Describe the morphology of the red blood cells.
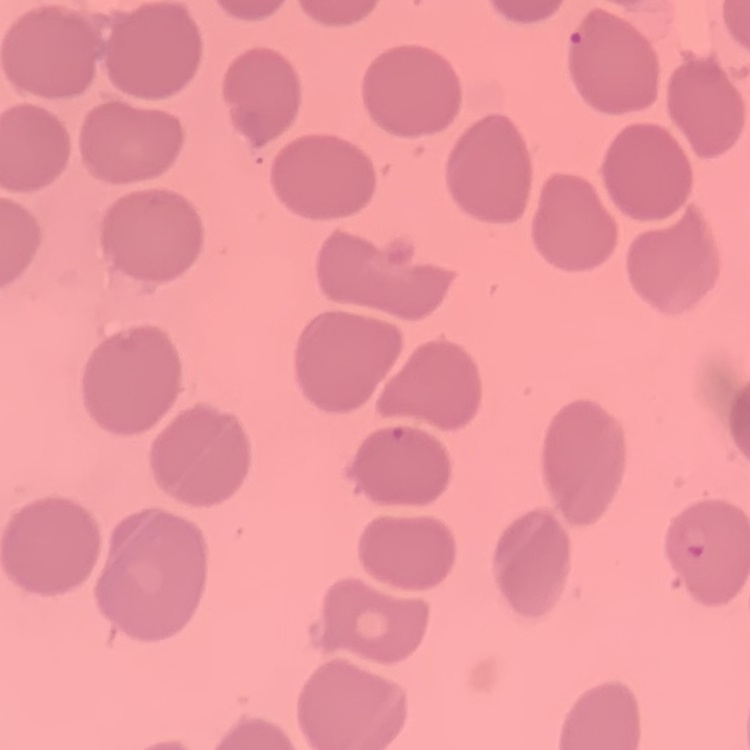
No rouleaux formation.

Summary:
  - Preparation: thin blood smear
  - Stain: Field's or Giemsa
  - Image type: square crop of a larger photomicrograph